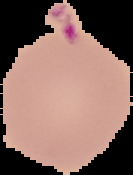 Image is 133×175 pixels. Segmented cell region on a black background. From a thin blood smear. Result: negative for Plasmodium parasites.